Comment on the morphology of the red blood cells.
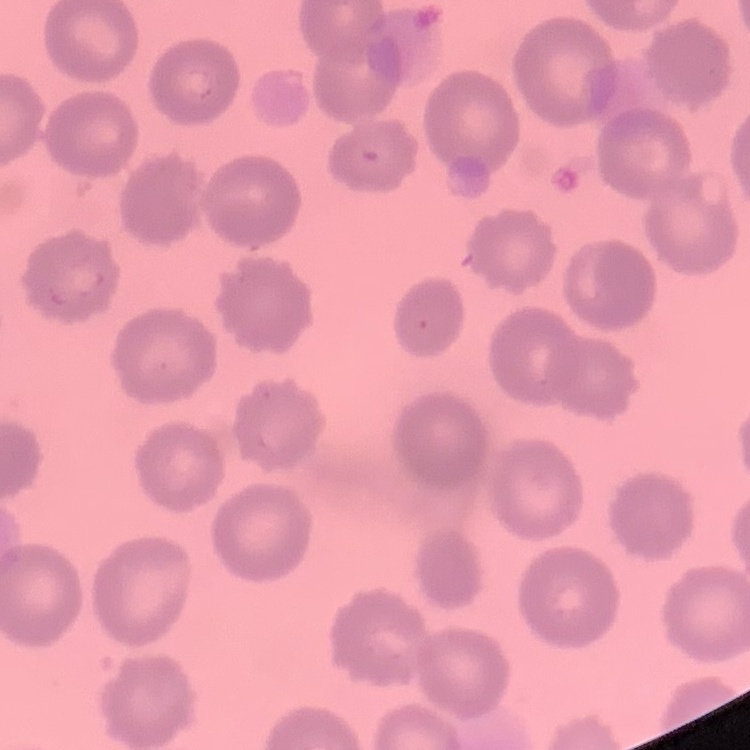

They show no rouleaux formation.

Thin blood smear. Field's or Giemsa stain. One tile cut from a larger photomicrograph.